State which parasite is depicted.
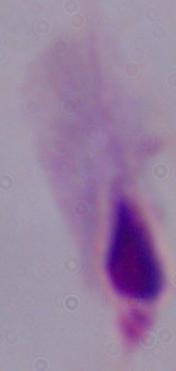

This is a trichomonad.

Summary:
  - Modality: photomicrograph
  - Magnification: 1000x